Name the cell type shown.
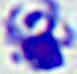
This is a leukocyte.

Summary:
  - Modality: micrograph
  - Magnification: 400x